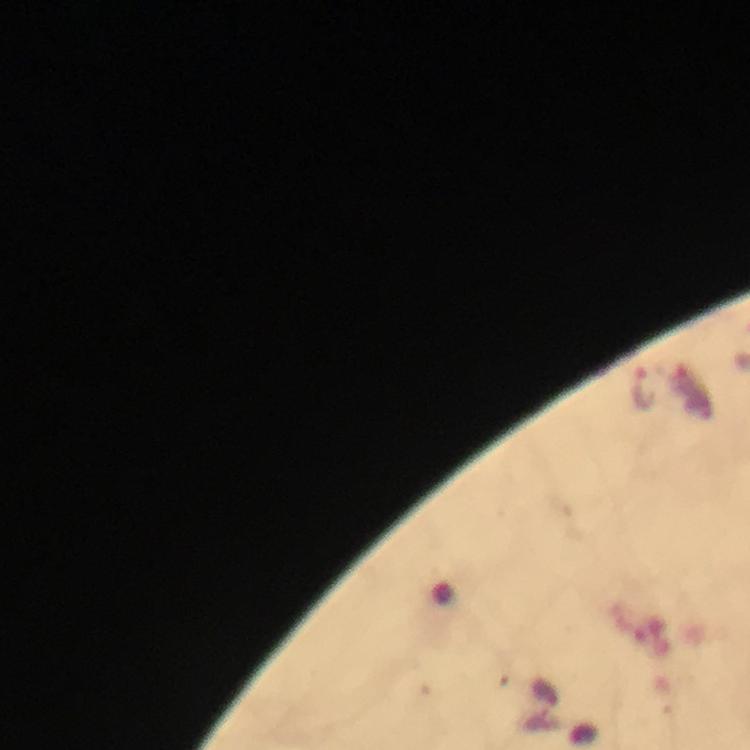

cropped_from: one field of view
image_size: 750×750 pixels
capture: smartphone photograph through a microscope
plasmodium_parasite_locations: 'approximate centers as (x, y) in pixels: (644, 388)'
preparation: thick blood smear
context: from a diagnostic examination for malaria
magnification: 100x
immersion_oil: applied
stain: Giemsa